Evaluate for Plasmodium parasites.
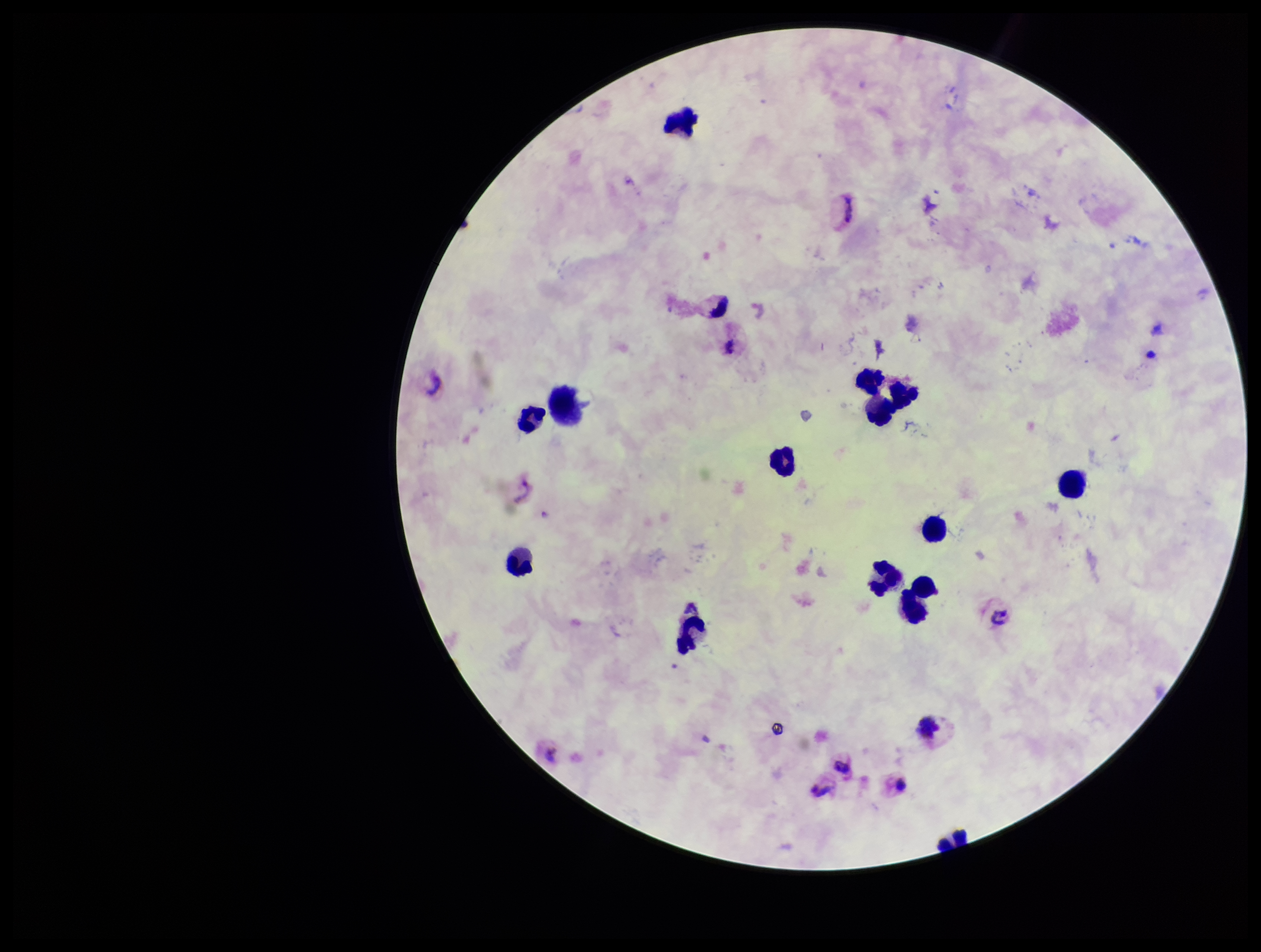

None detected.

Summary:
  - Patient malaria status: infected
  - Preparation: thick smear
  - Parasite count: 0
  - Capture: smartphone photograph through the microscope eyepiece
  - Leukocyte count: 13
  - Field of view: one from this slide
  - Stain: Giemsa
  - Species reported for this patient: Plasmodium vivax
  - Image size: 1261×952 pixels